Report the malaria status of this cell.
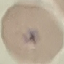

Uninfected.

{
  "stain": "Giemsa",
  "capture": "smartphone camera at the microscope eyepiece",
  "image_type": "cell patch, automatically extracted from a larger field of view and resized to 64 × 64 pixels",
  "preparation": "thin blood smear"
}